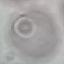
Summary:
  - Malaria status: uninfected
  - Capture: smartphone through the microscope eyepiece
  - Stain: Giemsa
  - Preparation: thin blood smear
  - Image type: automatically extracted cell patch, resized to 64 × 64 pixels